Give the preparation type.
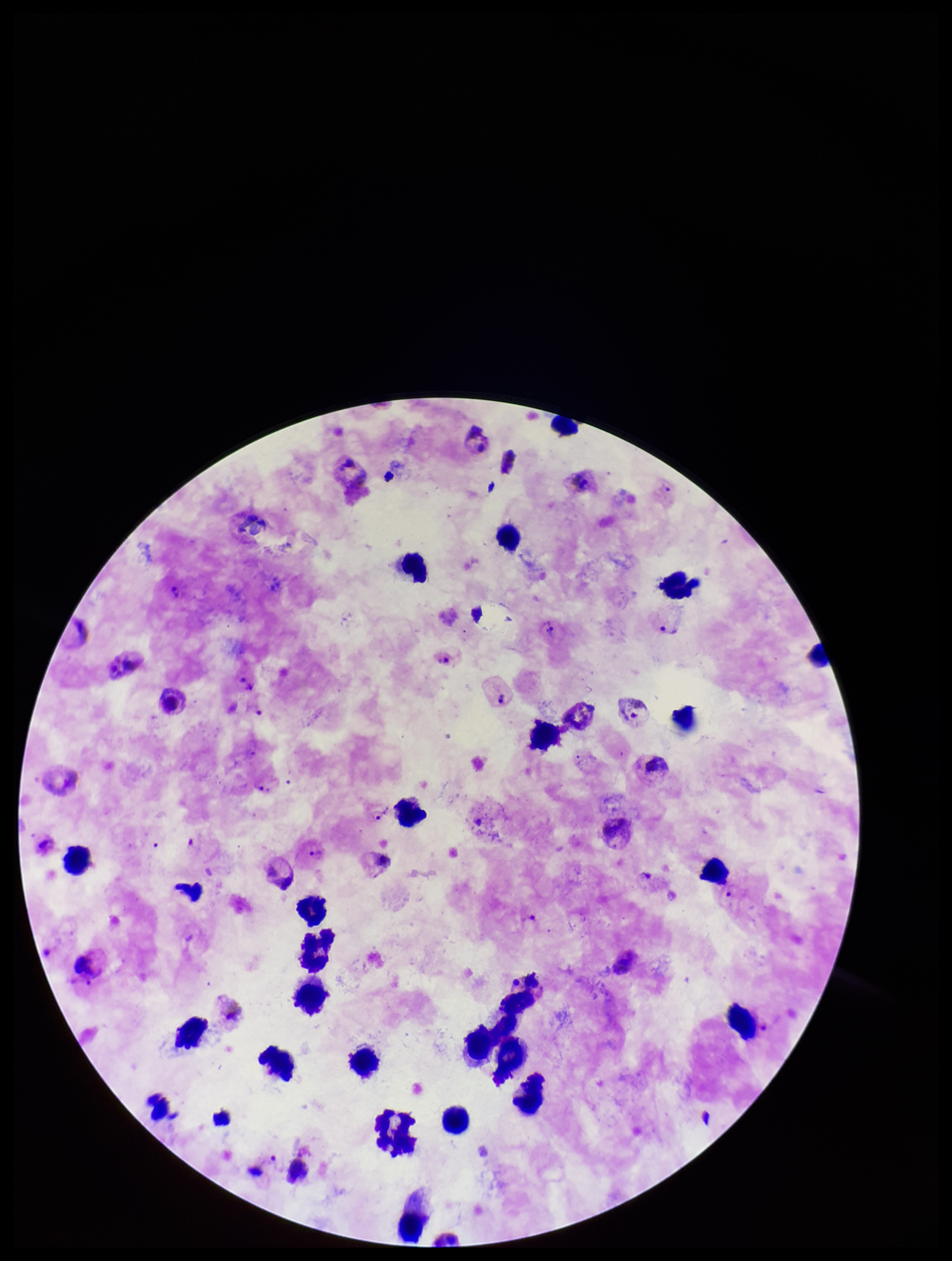

A thick smear.

Summary:
  - Stain: Giemsa
  - Parasite count: 6
  - Image size: 952×1261 pixels
  - Species reported for this patient: Plasmodium vivax
  - Leukocyte count: 27
  - Field of view: single
  - Patient malaria status: positive
  - Plasmodium parasites: seen
  - Capture: smartphone photograph through the microscope eyepiece